Locate every blood parasite and identify its species.
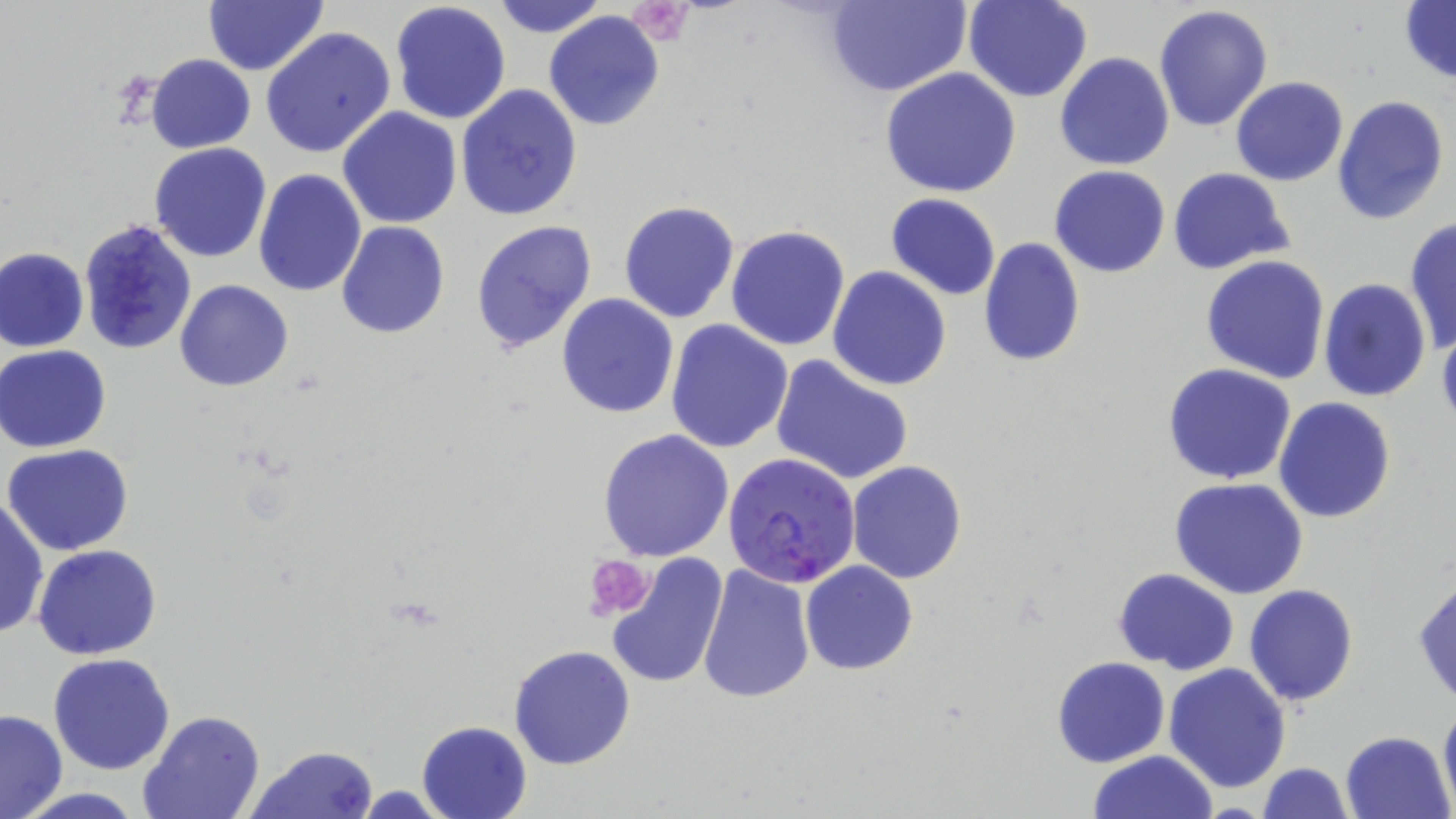
Approximate bounding boxes as (x1,y1)-(x2,y2) corner pairs in pixels.
Plasmodium falciparum-infected red blood cells: (722,454)-(861,588).
No Plasmodium ovale, Plasmodium malariae, Plasmodium vivax, Babesia divergens, or Trypanosoma brucei observed.

Uninfected red blood cell locations: (203,0)-(328,77), (491,0)-(608,38), (824,0)-(972,96), (964,0)-(1093,103), (389,1)-(511,124), (1400,1)-(1456,86), (1153,6)-(1274,131), (543,11)-(667,130), (260,26)-(398,160), (1054,51)-(1176,170), (146,53)-(255,154), (879,69)-(1021,197), (1230,77)-(1348,186), (456,84)-(584,221), (1332,95)-(1450,224), (337,107)-(462,229), (149,142)-(272,262), (1049,166)-(1172,278), (253,168)-(367,297), (1167,168)-(1295,273), (885,194)-(1002,300), (617,201)-(740,322), (1403,215)-(1455,354), (469,219)-(597,354), (336,220)-(449,338), (73,222)-(196,361), (726,224)-(852,351), (977,237)-(1085,369), (1,247)-(89,352), (1200,256)-(1331,386), (827,266)-(952,390), (1318,277)-(1432,403), (174,280)-(293,390), (556,294)-(680,419), (665,319)-(794,453), (0,344)-(111,453), (770,354)-(914,487), (1161,363)-(1297,484), (1273,397)-(1397,523), (597,429)-(734,561), (4,444)-(134,556), (845,461)-(968,585), (1169,477)-(1309,599), (1191,492)-(1329,671), (0,496)-(48,641), (32,544)-(163,660), (604,551)-(731,691), (801,561)-(919,674), (696,566)-(815,704), (1113,567)-(1240,674), (1413,575)-(1456,706), (1245,583)-(1359,704), (508,643)-(635,770), (48,653)-(176,775), (1051,657)-(1170,768), (1164,662)-(1291,793), (1438,699)-(1456,812), (0,707)-(68,819), (138,710)-(265,819), (417,720)-(532,819), (1339,731)-(1454,819), (247,745)-(378,819), (1089,749)-(1218,819), (1258,762)-(1353,819), (12,789)-(148,819). Platelet locations: (626,2)-(695,46), (586,555)-(653,624). Slide-level diagnosis: Plasmodium falciparum. One field of a larger specimen. Light microscopy. Image is 1456×819 pixels. Thin blood film. May-Grünwald-Giemsa stain. 1000x magnification.